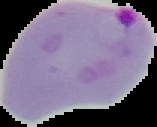
Summary:
  - Image size: 157×127 pixels
  - Image type: cell region segmented out of the field of view; surrounding area masked to black
  - Malaria status: parasitized
  - Preparation: thin blood smear